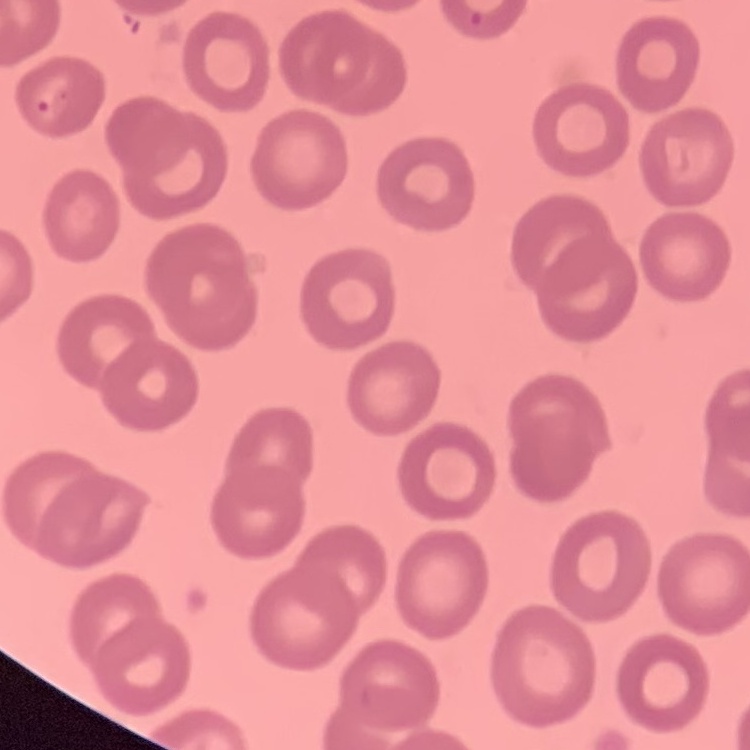
red blood cell morphology = no rouleaux formation
image type = one tile cut from a larger photomicrograph
stain = Field's or Giemsa
preparation = thin blood smear